Classify this cell by malaria status.
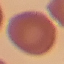
It is uninfected.

Giemsa stain. Thin smear of blood. Photographed with a smartphone camera at the microscope eyepiece. Automatically extracted cell patch, resized to 64 × 64 pixels.